State which parasite is depicted.
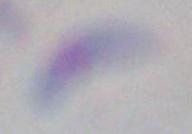
This is Toxoplasma gondii.

1000x magnification. Micrograph.